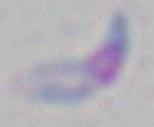

{
  "modality": "micrograph",
  "magnification": "1000x",
  "identification": "Toxoplasma gondii"
}